Name the parasite shown.
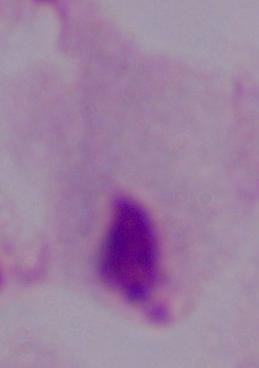
This is a trichomonad.

Summary:
  - Modality: micrograph
  - Magnification: 1000x